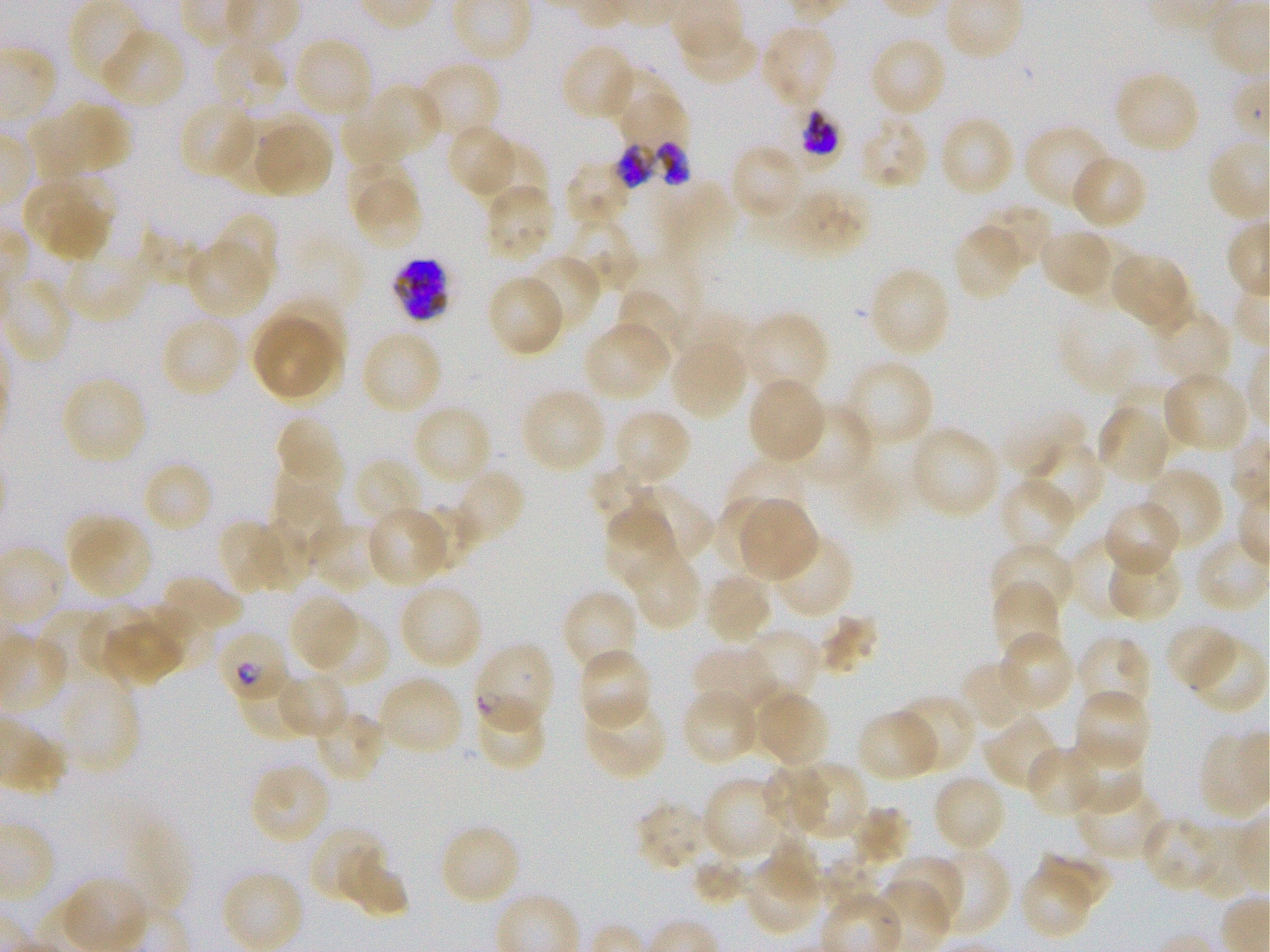

Approximate bounding boxes as [x1, y1, x2, y2] in pixels. Not every red blood cell is marked. A life-cycle stage — or a range of stages, where the recorded stages span more than one — follows each staged infected red blood cell.
Summary:
  - Locations of red blood cells of indeterminate infection status: [233, 662, 310, 742]
  - Locations of uninfected red blood cells: [678, 21, 762, 87], [759, 22, 838, 113], [100, 27, 187, 109], [868, 36, 949, 119], [293, 37, 373, 119], [212, 40, 289, 117], [560, 43, 637, 122], [415, 60, 500, 144], [614, 67, 676, 125], [1113, 70, 1201, 155], [379, 83, 441, 148], [618, 93, 696, 150], [343, 98, 413, 164], [30, 100, 132, 183], [179, 100, 257, 182], [223, 113, 297, 185], [856, 115, 930, 191], [938, 115, 1016, 198], [256, 124, 334, 198], [446, 124, 519, 199], [1022, 124, 1112, 213], [477, 139, 548, 210], [729, 144, 805, 223], [1070, 154, 1148, 231], [344, 160, 416, 226], [563, 160, 635, 229], [23, 176, 117, 263], [659, 180, 737, 250], [355, 181, 423, 251], [483, 183, 557, 264], [790, 190, 875, 254], [971, 206, 1054, 279], [217, 215, 280, 289], [558, 215, 638, 296], [952, 220, 1029, 301], [139, 225, 201, 287], [1038, 226, 1117, 301], [59, 239, 160, 324], [188, 245, 265, 317], [1109, 249, 1193, 332], [522, 255, 602, 335], [868, 266, 952, 358], [486, 274, 565, 357], [613, 287, 690, 364], [1059, 302, 1168, 399], [1151, 308, 1232, 386], [742, 310, 830, 399], [250, 312, 342, 402], [161, 314, 244, 398], [582, 319, 672, 403], [360, 329, 443, 416], [668, 334, 748, 422], [843, 358, 934, 449], [1162, 370, 1251, 454], [60, 376, 149, 465], [747, 377, 828, 465], [1115, 382, 1193, 452], [519, 387, 607, 474], [1096, 401, 1172, 487], [412, 404, 492, 487], [783, 405, 873, 490], [612, 409, 692, 488], [274, 413, 343, 490], [907, 424, 1001, 521], [1021, 439, 1105, 522], [271, 452, 344, 529], [351, 457, 424, 531], [141, 460, 215, 535], [730, 462, 808, 525], [591, 463, 654, 515], [1140, 466, 1224, 552], [452, 468, 526, 549], [998, 477, 1077, 555], [620, 484, 714, 566], [271, 489, 346, 566], [712, 497, 781, 572], [740, 498, 819, 582], [1102, 500, 1182, 577], [410, 503, 476, 573], [367, 505, 453, 585], [603, 506, 678, 591], [64, 513, 151, 602], [217, 518, 287, 593], [306, 519, 381, 592], [262, 527, 311, 594], [770, 534, 855, 620], [1076, 539, 1147, 620], [991, 542, 1076, 621], [1101, 544, 1183, 622], [626, 546, 702, 631], [703, 571, 774, 646], [159, 574, 244, 642], [992, 580, 1061, 663], [397, 581, 483, 671], [561, 589, 640, 674], [286, 591, 361, 673], [79, 601, 152, 668], [820, 612, 879, 672], [309, 613, 389, 688], [35, 614, 108, 679], [1164, 622, 1241, 690], [104, 624, 191, 688], [741, 628, 819, 706], [998, 631, 1076, 712], [1185, 634, 1268, 715], [1075, 635, 1151, 718], [693, 645, 779, 719], [576, 647, 652, 731], [957, 659, 1037, 733], [43, 668, 140, 775], [275, 671, 349, 738], [376, 675, 464, 758], [750, 687, 830, 769], [681, 689, 760, 765], [1074, 689, 1151, 770], [474, 695, 546, 772], [894, 695, 975, 776], [581, 696, 668, 781], [313, 708, 386, 784], [858, 709, 942, 783], [984, 714, 1064, 792], [1065, 736, 1145, 812], [1025, 744, 1103, 819], [760, 757, 831, 835], [797, 761, 868, 837], [250, 762, 332, 847], [931, 772, 1007, 854], [701, 775, 786, 862], [1074, 782, 1168, 860], [637, 802, 701, 868], [849, 807, 912, 869], [1144, 815, 1221, 892], [438, 823, 521, 906], [309, 827, 388, 898], [764, 836, 824, 902], [340, 846, 410, 918], [1037, 846, 1111, 905], [932, 847, 1010, 936], [742, 850, 823, 937], [884, 855, 966, 931], [691, 859, 750, 903], [822, 859, 880, 917], [1019, 870, 1089, 938]
  - Locations of infected red blood cells: [779, 107, 845, 172] late trophozoite to early schizont; [609, 137, 707, 192]; [392, 257, 448, 321]; [215, 630, 291, 707] early ring to early trophozoite; [473, 641, 555, 734]
  - Field of view: single
  - Objective: 100x, oil immersion, numerical aperture 1.25
  - Stain: Giemsa
  - Donor blood group: O+
  - Culture: in-vitro P. falciparum strain 3D7, static
  - Image size: 1270×952 pixels
  - Preparation: thin blood smear